Identify the cell.
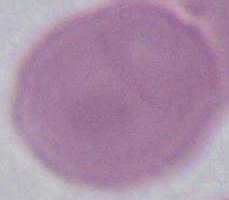

An erythrocyte.

modality = micrograph
magnification = 1000x